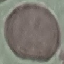
result: negative for malaria parasites
stain: Giemsa
capture: smartphone camera at the microscope eyepiece
preparation: thin blood film
image_type: cell patch, automatically extracted from a larger field of view and resized to 64 × 64 pixels